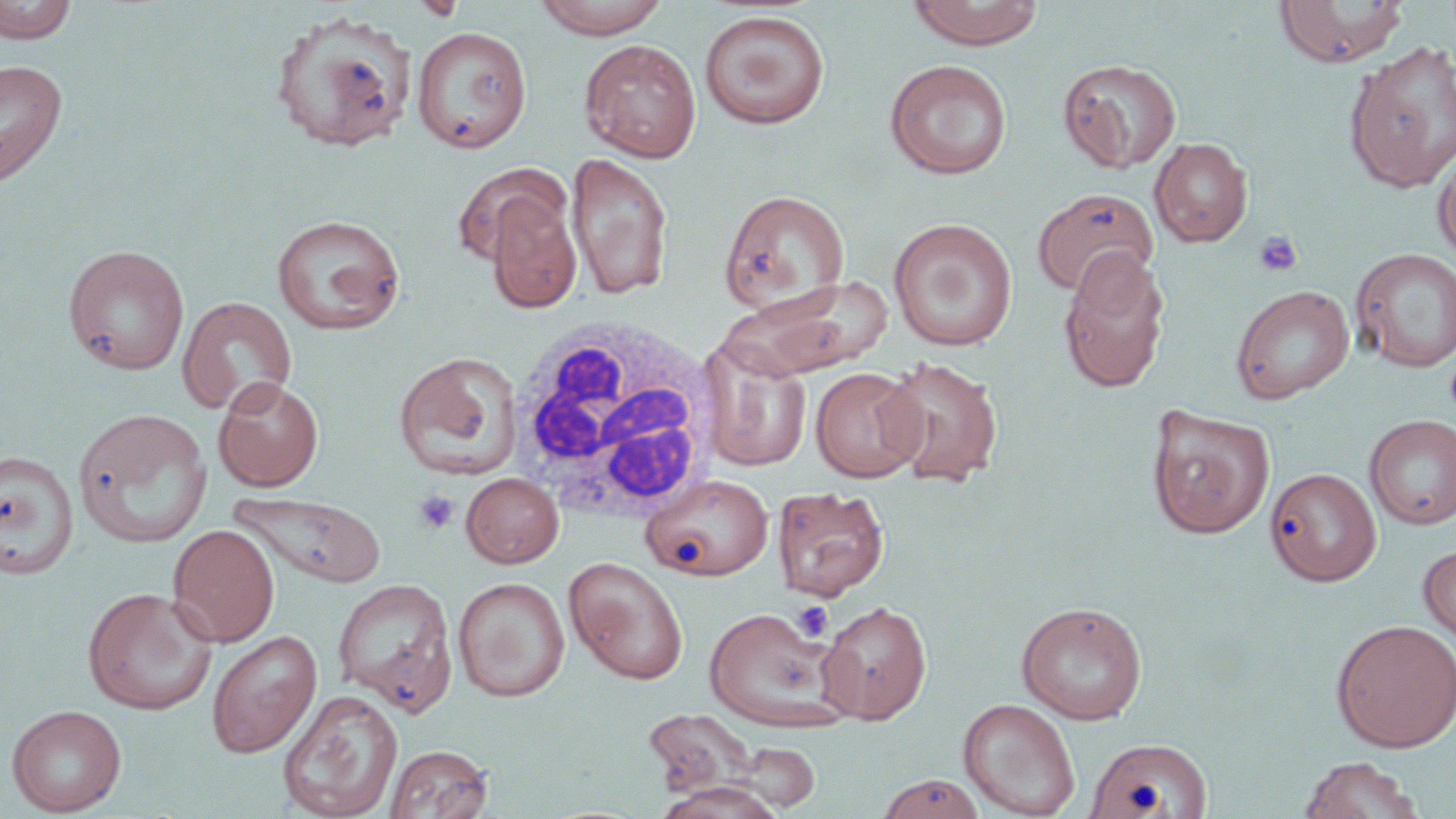
slide-level diagnosis = negative for blood parasites
image size = 1456×819 pixels
uninfected red blood cell locations = approximate bounding boxes as named x1/y1/x2/y2 corners in pixels: (x1=0, y1=0, x2=76, y2=45), (x1=410, y1=0, x2=468, y2=22), (x1=531, y1=0, x2=672, y2=38), (x1=907, y1=0, x2=1044, y2=49), (x1=1274, y1=1, x2=1410, y2=67), (x1=269, y1=10, x2=417, y2=153), (x1=699, y1=10, x2=830, y2=129), (x1=411, y1=26, x2=532, y2=153), (x1=579, y1=39, x2=702, y2=162), (x1=576, y1=41, x2=688, y2=292), (x1=1345, y1=41, x2=1456, y2=194), (x1=1057, y1=57, x2=1182, y2=173), (x1=1, y1=59, x2=68, y2=187), (x1=885, y1=59, x2=1012, y2=179), (x1=1150, y1=137, x2=1252, y2=247), (x1=1433, y1=144, x2=1456, y2=264), (x1=566, y1=151, x2=672, y2=300), (x1=453, y1=161, x2=570, y2=265), (x1=1033, y1=187, x2=1158, y2=297), (x1=718, y1=188, x2=849, y2=316), (x1=485, y1=195, x2=582, y2=314), (x1=271, y1=214, x2=406, y2=335), (x1=888, y1=217, x2=1018, y2=351), (x1=62, y1=243, x2=190, y2=374), (x1=1058, y1=247, x2=1170, y2=393), (x1=1351, y1=248, x2=1456, y2=373), (x1=735, y1=278, x2=894, y2=376), (x1=1230, y1=284, x2=1354, y2=405), (x1=177, y1=295, x2=297, y2=416), (x1=698, y1=340, x2=813, y2=472), (x1=393, y1=351, x2=523, y2=481), (x1=879, y1=355, x2=1005, y2=487), (x1=810, y1=367, x2=926, y2=483), (x1=213, y1=376, x2=324, y2=491), (x1=1146, y1=404, x2=1275, y2=538), (x1=73, y1=407, x2=214, y2=549), (x1=1364, y1=415, x2=1456, y2=529), (x1=0, y1=449, x2=79, y2=581), (x1=1265, y1=467, x2=1381, y2=586), (x1=461, y1=473, x2=563, y2=568), (x1=641, y1=474, x2=774, y2=581), (x1=772, y1=485, x2=889, y2=601), (x1=229, y1=490, x2=387, y2=588), (x1=167, y1=524, x2=280, y2=647), (x1=1418, y1=543, x2=1456, y2=647), (x1=563, y1=556, x2=689, y2=685), (x1=332, y1=577, x2=458, y2=717), (x1=453, y1=577, x2=570, y2=702), (x1=82, y1=586, x2=218, y2=714), (x1=816, y1=600, x2=932, y2=724), (x1=1016, y1=602, x2=1147, y2=725), (x1=702, y1=606, x2=848, y2=731), (x1=1331, y1=619, x2=1456, y2=752), (x1=207, y1=630, x2=322, y2=759), (x1=278, y1=689, x2=403, y2=818), (x1=958, y1=698, x2=1080, y2=819), (x1=6, y1=703, x2=127, y2=816), (x1=641, y1=709, x2=764, y2=801), (x1=1090, y1=741, x2=1216, y2=819), (x1=384, y1=744, x2=494, y2=819), (x1=1297, y1=755, x2=1426, y2=819), (x1=875, y1=773, x2=985, y2=818), (x1=657, y1=781, x2=784, y2=818)
preparation = thin blood smear
field of view = one of a larger specimen
platelet locations = approximate bounding boxes as named x1/y1/x2/y2 corners in pixels: (x1=410, y1=0, x2=469, y2=21), (x1=1254, y1=229, x2=1303, y2=277), (x1=413, y1=490, x2=459, y2=534), (x1=792, y1=601, x2=833, y2=641)
modality = light microscopy
white blood cell locations = approximate bounding boxes as named x1/y1/x2/y2 corners in pixels: (x1=501, y1=317, x2=724, y2=528)
stain = May-Grünwald-Giemsa
magnification = 1000x